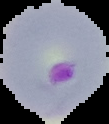

image size = 109×124 pixels
preparation = thin blood film
malaria status = parasitized
image type = cell region segmented out of the field of view; surrounding area masked to black